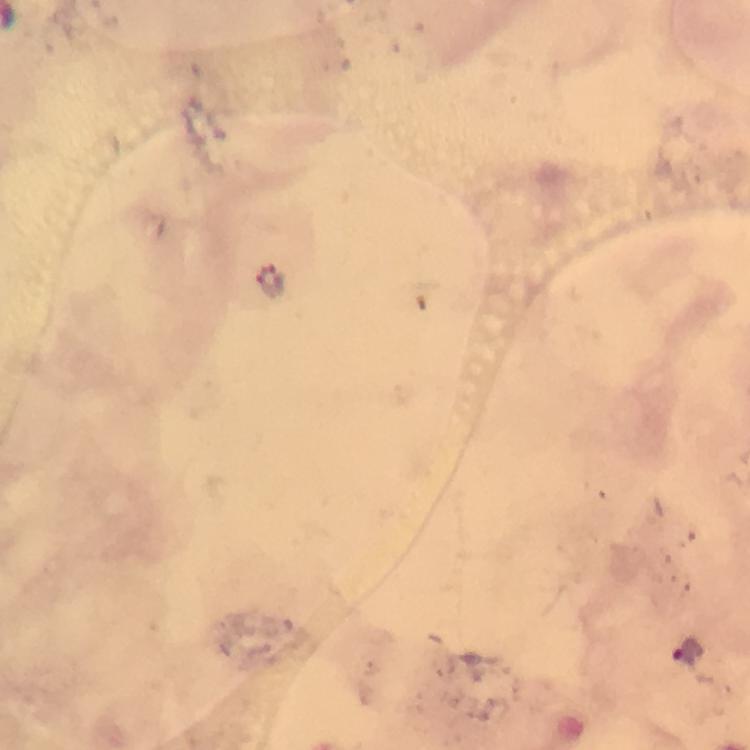
Approximate centers as {x, y} in pixels.
Summary:
  - Plasmodium parasite locations: {687, 654}
  - Magnification: 100x
  - Image size: 750×750 pixels
  - Preparation: thick blood film
  - Cropped from: a single field of view
  - Context: from a diagnostic examination for malaria
  - Immersion oil: applied
  - Stain: Giemsa
  - Capture: smartphone camera through the microscope